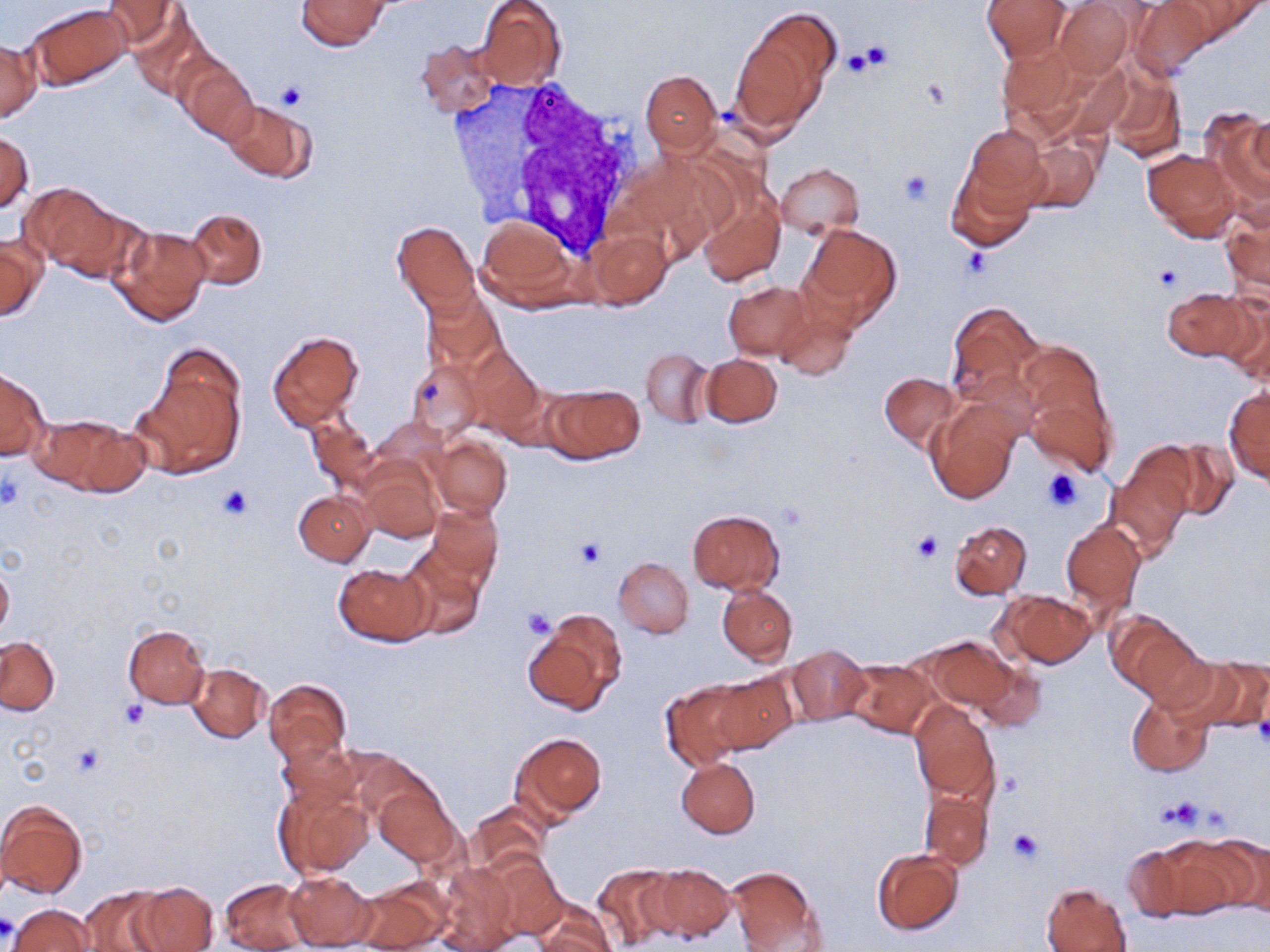

slide_level_diagnosis: negative for blood parasites
preparation: thin blood smear
image_size: 1270×952 pixels
modality: light microscopy
field_of_view: single
stain: May-Grünwald-Giemsa
white_blood_cell_locations: 'approximate bounding boxes as (x1, y1, x2, y2) in pixels: (447, 75, 651, 256)'
magnification: 1000x
platelet_locations: 'approximate bounding boxes as (x1, y1, x2, y2) in pixels: (848, 42, 892, 76), (921, 78, 953, 111), (277, 81, 307, 111), (900, 171, 932, 206), (1155, 266, 1184, 291), (421, 381, 445, 408), (1040, 467, 1086, 513), (0, 473, 21, 510), (216, 484, 255, 521), (775, 499, 808, 529), (911, 531, 944, 564), (575, 537, 604, 567), (518, 605, 557, 639), (120, 700, 147, 729), (1255, 706, 1270, 750), (71, 744, 106, 778), (1160, 797, 1205, 829), (1008, 828, 1045, 863), (0, 914, 17, 945)'
uninfected_red_blood_cell_locations: 'approximate bounding boxes as (x1, y1, x2, y2) in pixels: (102, 0, 179, 50), (297, 0, 392, 50), (982, 0, 1071, 64), (1175, 0, 1265, 45), (476, 1, 567, 90), (1054, 1, 1135, 78), (1128, 1, 1214, 81), (29, 4, 130, 89), (127, 10, 212, 99), (732, 10, 838, 131), (417, 38, 500, 118), (0, 39, 41, 122), (995, 39, 1108, 144), (176, 57, 257, 140), (1104, 67, 1185, 165), (641, 69, 720, 153), (225, 99, 314, 182), (1206, 110, 1268, 212), (965, 124, 1047, 207), (0, 131, 33, 211), (1020, 137, 1101, 216), (1142, 147, 1239, 240), (775, 163, 864, 236), (946, 163, 1036, 252), (695, 182, 786, 285), (21, 184, 124, 273), (1220, 202, 1270, 300), (186, 208, 266, 289), (477, 217, 576, 307), (391, 220, 479, 310), (798, 222, 903, 328), (110, 225, 212, 326), (587, 228, 671, 308), (1, 233, 46, 322), (724, 281, 811, 360), (424, 287, 503, 372), (1162, 287, 1254, 360), (1218, 289, 1270, 383), (773, 299, 857, 382), (945, 300, 1044, 406), (267, 330, 364, 430), (1014, 343, 1118, 476), (462, 344, 542, 435), (641, 348, 712, 427), (702, 353, 781, 427), (136, 354, 246, 477), (407, 360, 486, 441), (0, 369, 48, 459), (879, 372, 959, 450), (546, 383, 643, 461), (1223, 386, 1270, 486), (925, 400, 1022, 506), (34, 414, 144, 497), (306, 416, 380, 496), (429, 434, 512, 518), (1156, 439, 1240, 518), (1107, 454, 1191, 558), (357, 460, 442, 543), (294, 490, 373, 564), (428, 503, 503, 584), (688, 506, 783, 597), (949, 520, 1032, 598), (1061, 520, 1145, 616), (397, 546, 487, 641), (614, 557, 694, 638), (0, 560, 13, 640), (335, 561, 431, 646), (717, 585, 796, 664), (992, 590, 1097, 669), (1109, 611, 1203, 700), (523, 612, 627, 715), (123, 624, 210, 708), (926, 636, 1017, 715), (0, 638, 60, 715), (785, 644, 869, 726), (972, 657, 1048, 732), (1179, 657, 1269, 732), (845, 660, 940, 737), (188, 663, 270, 742), (710, 671, 797, 754), (264, 678, 352, 768), (658, 679, 756, 769), (1128, 694, 1213, 776), (910, 701, 999, 804), (512, 732, 608, 820), (278, 737, 361, 812), (676, 757, 760, 837), (274, 780, 372, 880), (374, 783, 460, 868), (921, 790, 993, 870), (0, 800, 88, 901), (467, 801, 548, 876), (1153, 834, 1260, 916), (1208, 835, 1270, 916), (1119, 839, 1208, 922), (872, 849, 964, 935), (488, 855, 567, 938), (435, 861, 521, 952), (592, 863, 680, 950), (647, 863, 735, 943), (727, 865, 825, 951), (282, 869, 376, 951), (220, 877, 310, 952), (351, 880, 451, 952), (133, 881, 218, 952), (1041, 883, 1130, 952), (79, 887, 172, 952), (530, 902, 616, 952), (9, 904, 97, 951)'